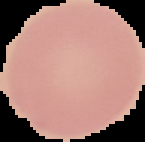
Segmented cell region on a black background. Image is 145×142 pixels. Malaria status: uninfected. From a thin blood smear.